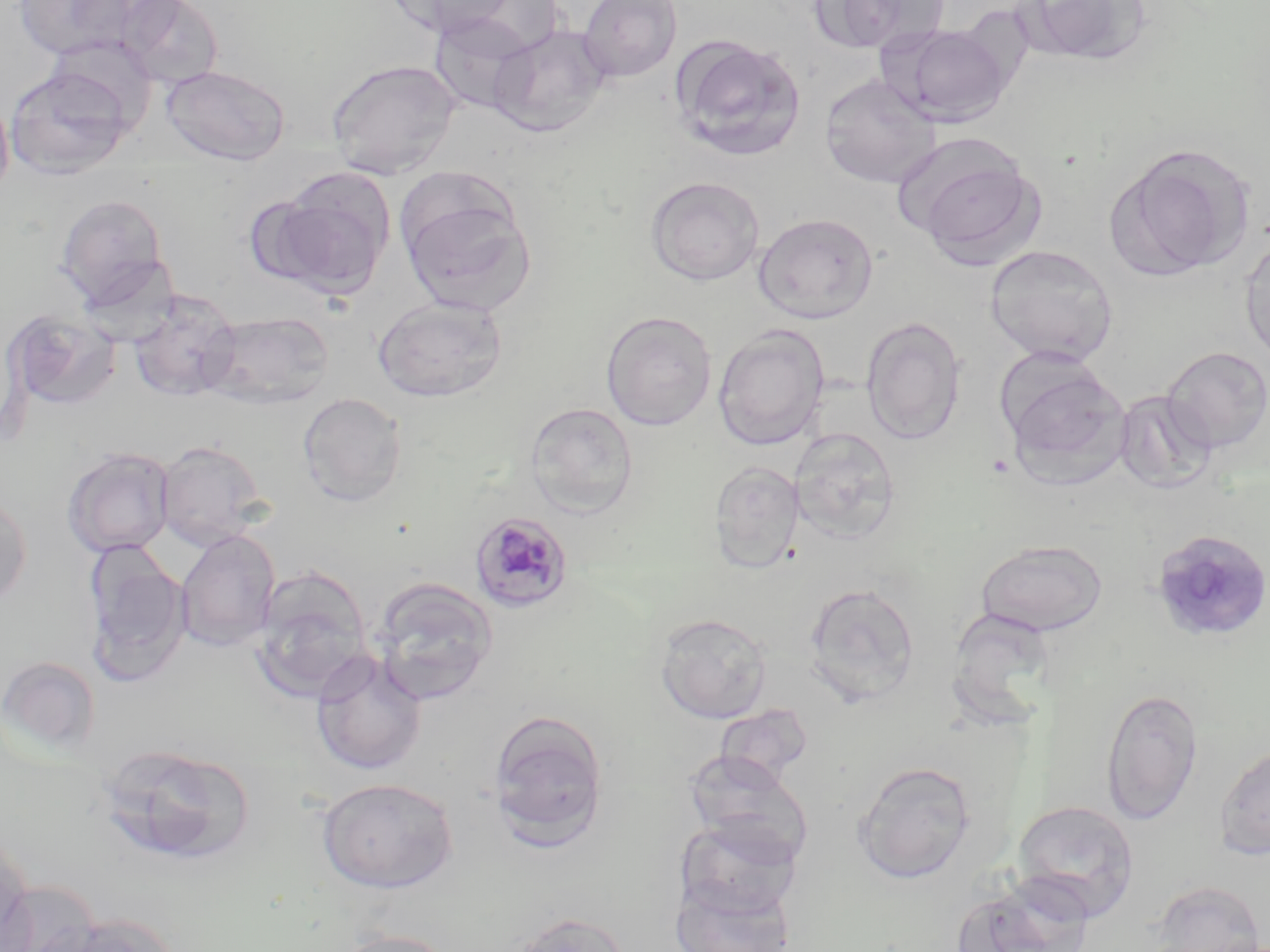 Approximate bounding boxes as (x1,y1)-(x2,y2) corner pairs in pixels. Uninfected red blood cell locations: (11,0)-(143,60), (118,0)-(224,89), (385,0)-(519,38), (578,0)-(682,83), (808,0)-(947,54), (1020,0)-(1154,66), (429,13)-(537,116), (488,24)-(611,138), (884,24)-(1014,127), (669,33)-(806,161), (43,35)-(159,135), (326,58)-(461,180), (161,64)-(290,166), (4,66)-(133,180), (820,74)-(941,189), (0,88)-(14,203), (898,134)-(1043,266), (1110,143)-(1255,279), (267,170)-(395,297), (645,176)-(765,286), (399,184)-(538,317), (54,193)-(171,308), (753,212)-(879,323), (1239,234)-(1270,368), (985,244)-(1119,366), (127,288)-(243,403), (372,295)-(508,403), (7,309)-(122,411), (202,310)-(335,409), (600,310)-(718,431), (861,316)-(966,445), (713,324)-(830,451), (1161,346)-(1270,453), (1002,363)-(1133,491), (1113,390)-(1217,495), (297,392)-(408,507), (523,401)-(639,519), (789,427)-(901,545), (154,440)-(268,551), (62,448)-(175,558), (708,460)-(804,573), (0,492)-(32,609), (1150,528)-(1270,643), (176,529)-(281,652), (974,539)-(1109,637), (82,540)-(190,684), (250,566)-(372,701), (370,576)-(498,704), (801,582)-(921,707), (655,612)-(772,723), (310,650)-(428,776), (0,655)-(101,756), (1100,685)-(1204,826), (714,704)-(814,787), (487,710)-(610,849), (1214,741)-(1270,861), (95,742)-(255,868), (684,751)-(813,865), (853,760)-(976,884), (316,777)-(458,894), (1012,799)-(1140,921), (674,817)-(801,924), (0,837)-(34,951), (668,876)-(796,952), (1151,879)-(1266,952), (947,880)-(1088,952), (34,911)-(179,952), (508,911)-(631,952), (330,929)-(460,952). Plasmodium malariae-infected red blood cell locations: (472,511)-(577,614). Slide-level diagnosis: Plasmodium malariae. Image is 1270×952 pixels. Optical microscopy. 1000x magnification. One field of a larger specimen. May-Grünwald-Giemsa stain. Thin blood smear.